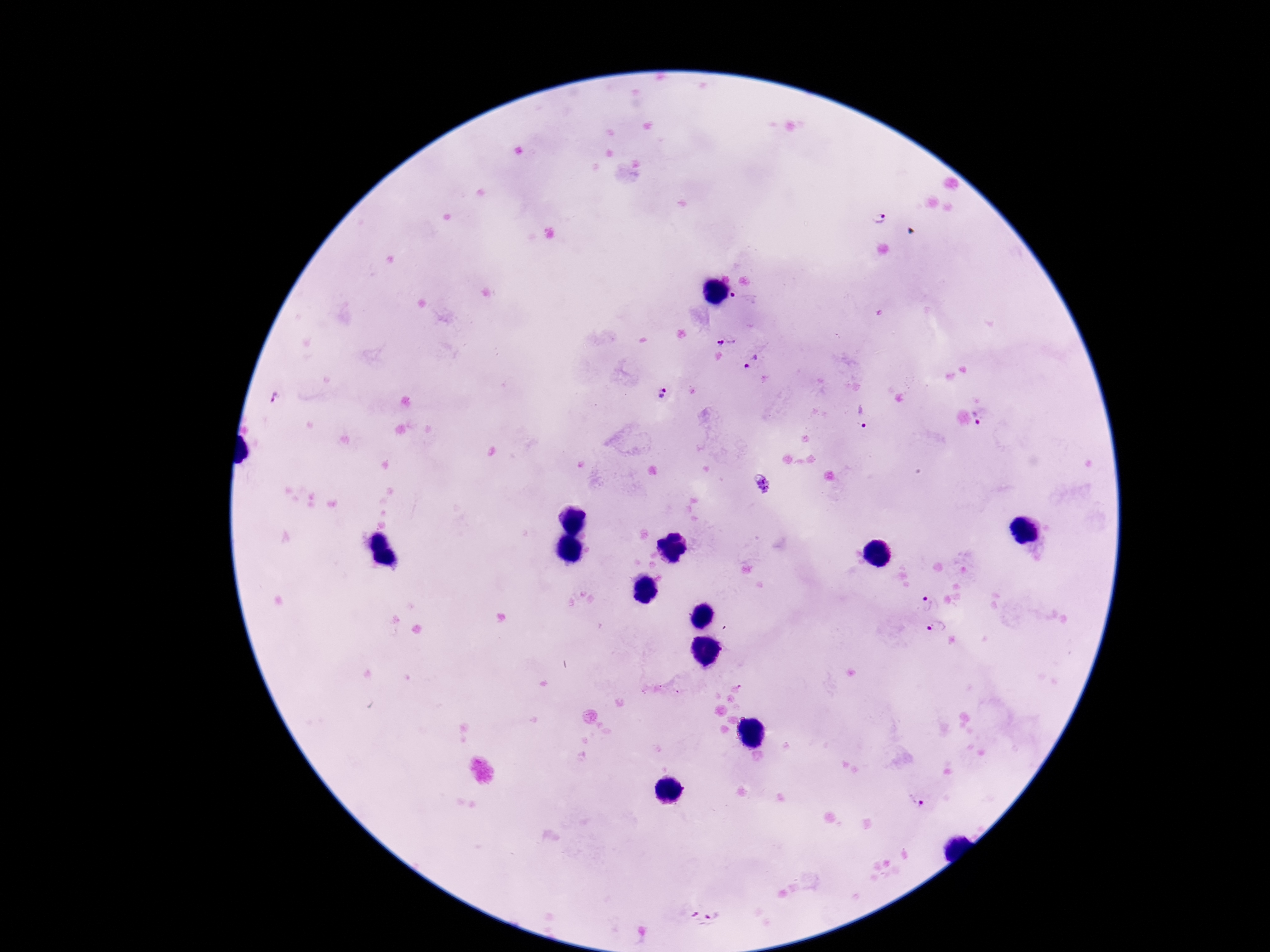
Approximate centers as {x, y} in pixels. Plasmodium parasite locations: {876, 221}, {727, 340}, {752, 361}, {664, 394}, {278, 399}, {861, 416}, {979, 417}, {761, 485}, {927, 604}, {936, 627}, {915, 799}, {713, 918}, {696, 919}. One field from this slide. Patient malaria status: positive. Giemsa-stained preparation. 100x magnification. Image is 1270×952 pixels. Smartphone photograph taken through the microscope eyepiece. Thick blood film.